Classify this cell by malaria status.
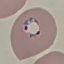

It is parasitized.

Giemsa stain. Acquired by smartphone through the microscope eyepiece. Cell patch, automatically extracted from a larger field of view and resized to 64 × 64 pixels. Thin smear of blood.